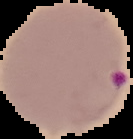 From a thin blood smear. Image is 133×139 pixels. The area outside the segmented cell region is set to black. Malaria status: parasitized.